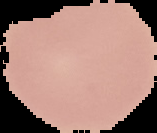
malaria status = uninfected
preparation = thin blood film
image size = 157×133 pixels
image type = cell region segmented out of the field of view; surrounding area masked to black